State which parasite is depicted.
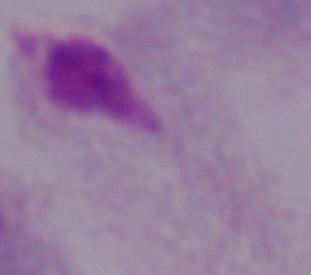
This is a trichomonad.

Summary:
  - Modality: micrograph
  - Magnification: 1000x